Assess this cell for malaria.
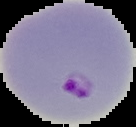

It is parasitized.

Image is 136×127 pixels. The area outside the segmented cell region is set to black. From a thin blood film.